Assess the morphology of the red blood cells.
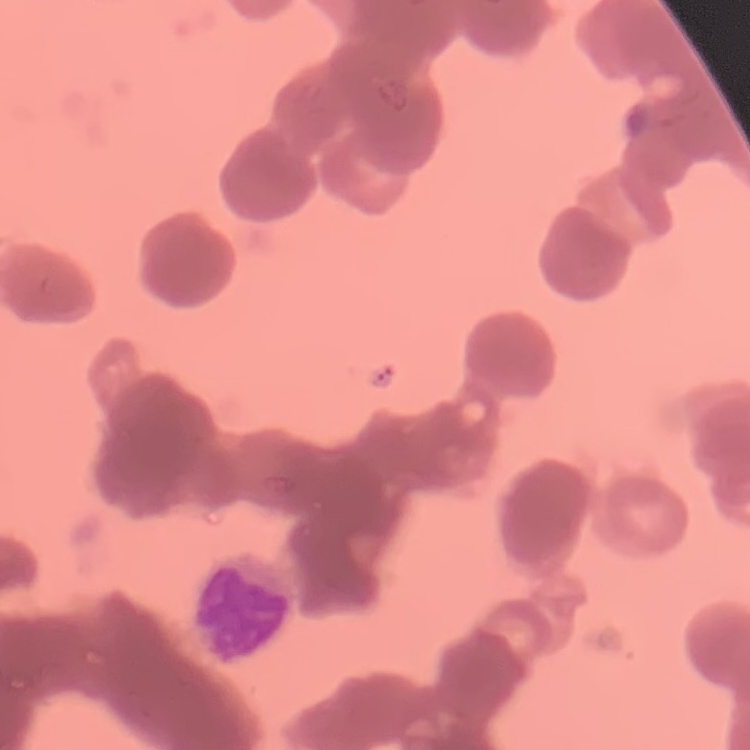

They show rouleaux formation.

Summary:
  - Stain: Field's or Giemsa
  - Preparation: thin blood film
  - Image type: square crop of a larger photomicrograph